Comment on the morphology of the red blood cells.
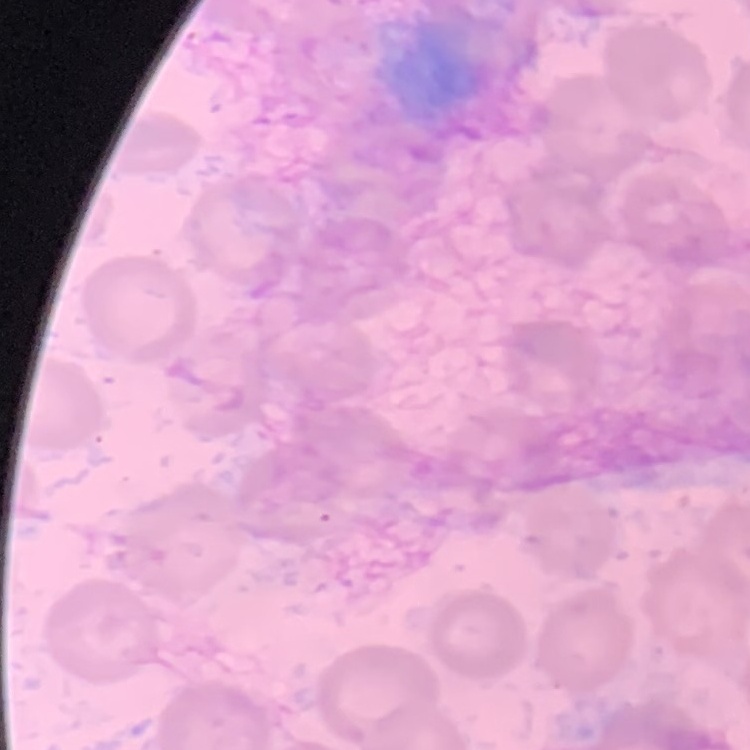
No rouleaux formation.

Summary:
  - Stain: Field's or Giemsa
  - Image type: square crop of a larger photomicrograph
  - Preparation: thin blood film